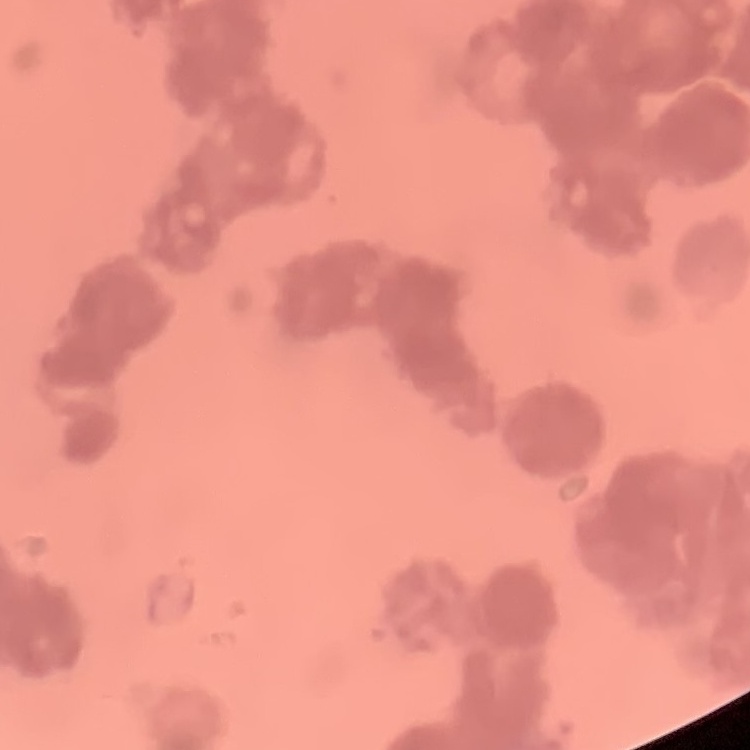
erythrocyte_morphology: rouleaux formation
image_type: square crop of a larger photomicrograph
preparation: thin blood film
stain: Field's or Giemsa